Assess this cell for malaria.
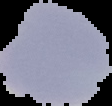

Uninfected.

Summary:
  - Image size: 112×106 pixels
  - Preparation: thin blood film
  - Image type: segmented cell region with the area outside set to black